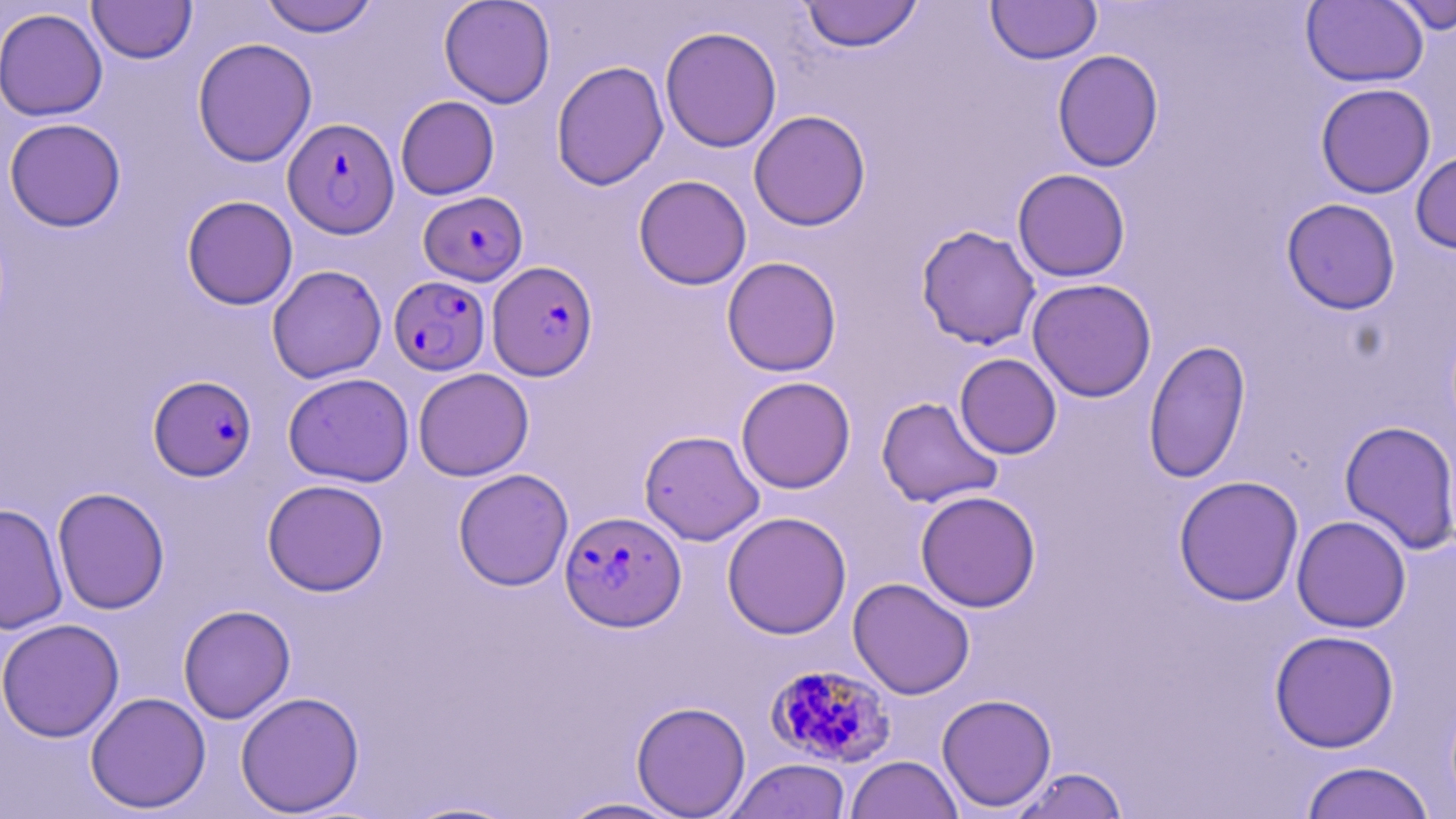
Approximate bounding boxes as (x1,y1)-(x2,y2) corner pairs in pixels. Uninfected red blood cell locations: (87,0)-(197,64), (259,0)-(379,37), (438,0)-(556,108), (799,0)-(924,53), (986,0)-(1102,65), (1301,0)-(1428,88), (1386,0)-(1456,34), (0,7)-(108,121), (660,26)-(782,153), (192,37)-(317,167), (1052,49)-(1164,172), (551,60)-(669,191), (1315,83)-(1436,198), (395,96)-(499,199), (748,110)-(871,231), (4,117)-(126,232), (1411,149)-(1456,254), (1012,168)-(1131,282), (633,174)-(752,290), (182,195)-(298,310), (1281,198)-(1401,315), (916,225)-(1041,350), (721,257)-(842,377), (266,265)-(386,383), (1027,277)-(1157,402), (1144,338)-(1251,484), (954,353)-(1062,459), (413,368)-(534,481), (283,372)-(414,487), (736,376)-(855,493), (876,396)-(1003,508), (1338,420)-(1456,554), (639,429)-(764,545), (453,468)-(574,590), (1173,475)-(1304,606), (262,479)-(389,596), (52,487)-(170,615), (915,490)-(1041,613), (0,503)-(68,635), (722,511)-(852,639), (1291,515)-(1411,633), (848,577)-(975,699), (178,604)-(295,723), (0,619)-(125,742), (1269,629)-(1399,753), (85,691)-(211,814), (235,691)-(364,816), (936,693)-(1057,813), (631,701)-(751,818), (845,755)-(963,819), (724,758)-(852,819), (1299,760)-(1436,819), (1008,766)-(1129,819), (555,797)-(690,818), (399,799)-(525,818). Plasmodium falciparum-infected red blood cell locations: (283,117)-(399,239), (419,191)-(528,286), (487,261)-(597,381), (389,275)-(490,375), (148,375)-(257,481), (561,514)-(687,636), (766,663)-(896,768). Slide-level diagnosis: Plasmodium falciparum. Thin blood film. May-Grünwald-Giemsa-stained preparation. Light microscopy. Image is 1456×819 pixels. One field of a larger specimen. 1000x magnification.